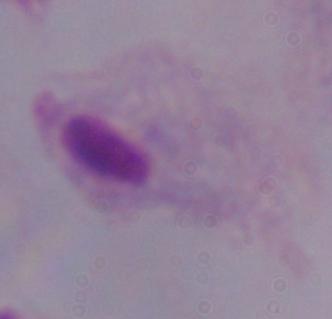

Summary:
  - Magnification: 1000x
  - Modality: micrograph
  - Identification: trichomonad